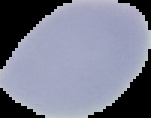

image_type: segmented cell region with the area outside set to black
malaria_status: uninfected
image_size: 151×118 pixels
preparation: thin blood smear